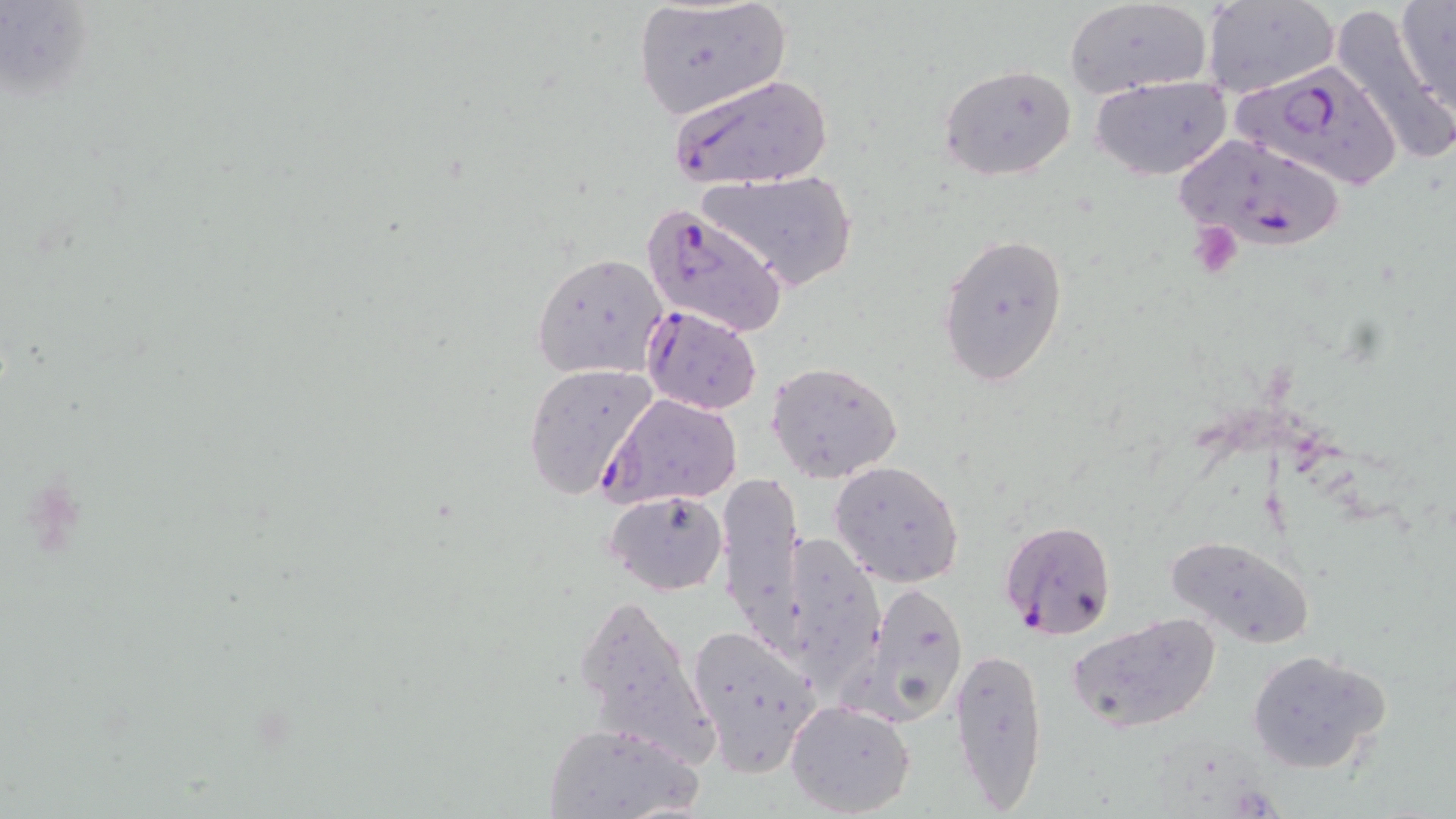
Plasmodium falciparum-infected red blood cell locations = approximate bounding boxes as (x1, y1, x2, y2) in pixels: (1232, 60, 1402, 191), (668, 74, 833, 189), (1172, 135, 1348, 259), (641, 202, 789, 338), (638, 305, 763, 414), (601, 392, 744, 508), (1000, 520, 1116, 640)
slide-level diagnosis = Plasmodium falciparum
preparation = thin blood film
image size = 1456×819 pixels
field of view = one of a larger specimen
magnification = 1000x
stain = May-Grünwald-Giemsa
uninfected red blood cell locations = approximate bounding boxes as (x1, y1, x2, y2) in pixels: (1200, 0, 1338, 99), (1395, 0, 1456, 115), (1063, 1, 1213, 100), (630, 2, 793, 121), (1329, 5, 1455, 169), (939, 64, 1078, 182), (1091, 75, 1231, 180), (699, 171, 859, 293), (936, 231, 1069, 386), (532, 252, 669, 379), (767, 360, 903, 484), (522, 363, 659, 500), (830, 460, 964, 587), (719, 474, 806, 645), (604, 489, 729, 596), (766, 528, 884, 696), (1167, 535, 1315, 649), (856, 580, 969, 725), (571, 588, 714, 764), (1065, 612, 1223, 735), (685, 623, 824, 776), (949, 645, 1048, 812), (1245, 647, 1392, 775), (786, 700, 915, 816), (541, 721, 702, 818)
modality = optical microscopy
platelet locations = approximate bounding boxes as (x1, y1, x2, y2) in pixels: (1189, 223, 1242, 280)